Report the malaria status of this cell.
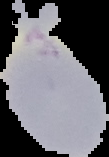
It is uninfected.

image size = 109×157 pixels
image type = cell region segmented out of the field of view; surrounding area masked to black
preparation = thin blood film